Report the malaria status of this cell.
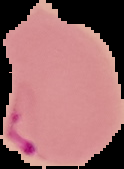
It is parasitized.

preparation: thin blood smear
image_type: segmented cell region with the area outside set to black
image_size: 124×169 pixels